Assess this cell for malaria.
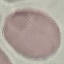

Uninfected.

Giemsa-stained preparation. Photographed with a smartphone camera at the microscope eyepiece. Cell patch, automatically extracted from a larger field of view and resized to 64 × 64 pixels. Thin blood smear.